Assess the morphology of the red blood cells.
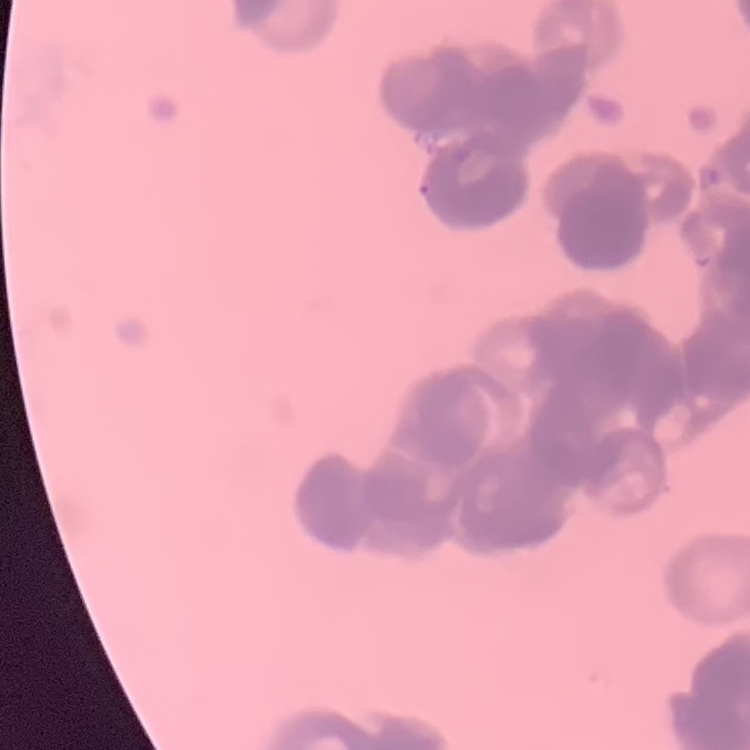
They show rouleaux formation.

One tile cut from a larger photomicrograph. Field's or Giemsa stain. Thin blood smear.